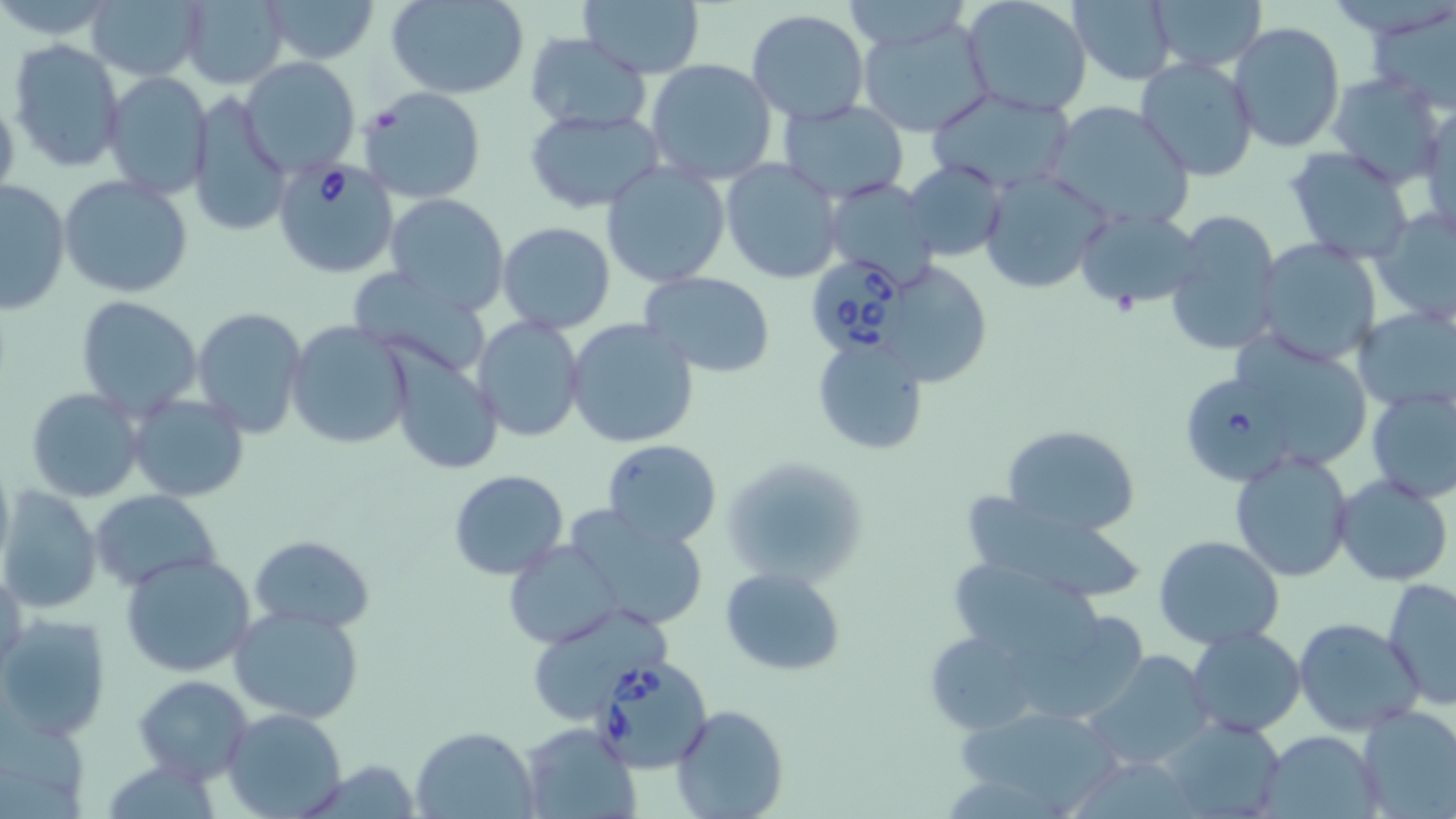 Approximate bounding boxes as [x1, y1, x2, y2] in pixels. Uninfected red blood cell locations: [84, 0, 208, 82], [179, 0, 289, 87], [262, 0, 378, 65], [387, 0, 530, 98], [960, 0, 1093, 117], [1067, 0, 1178, 86], [1151, 0, 1265, 72], [578, 1, 706, 77], [1367, 3, 1454, 114], [746, 10, 871, 125], [857, 13, 996, 138], [1229, 21, 1345, 153], [525, 34, 651, 133], [7, 38, 126, 172], [1134, 55, 1259, 183], [241, 57, 360, 174], [645, 58, 777, 186], [102, 70, 213, 198], [1328, 73, 1448, 190], [361, 87, 486, 204], [187, 90, 291, 236], [924, 90, 1078, 194], [0, 92, 20, 206], [778, 99, 911, 201], [1042, 101, 1196, 233], [1417, 103, 1455, 243], [524, 108, 666, 214], [1284, 145, 1419, 266], [722, 158, 846, 284], [903, 160, 1007, 261], [601, 162, 731, 287], [980, 171, 1111, 294], [59, 175, 194, 300], [0, 178, 71, 314], [823, 178, 941, 290], [385, 194, 508, 311], [1072, 207, 1204, 314], [1370, 207, 1456, 328], [1164, 209, 1284, 358], [497, 222, 617, 333], [1254, 238, 1384, 367], [895, 263, 989, 380], [349, 268, 490, 373], [641, 272, 775, 376], [75, 296, 203, 419], [1351, 305, 1456, 414], [192, 307, 307, 438], [473, 316, 587, 442], [565, 318, 699, 449], [287, 321, 414, 451], [1223, 333, 1383, 476], [810, 334, 928, 456], [386, 345, 504, 478], [25, 386, 145, 504], [1365, 388, 1456, 504], [128, 393, 250, 503], [1003, 424, 1140, 536], [602, 439, 722, 548], [1230, 450, 1355, 584], [0, 452, 15, 578], [722, 461, 857, 622], [447, 469, 570, 581], [1333, 474, 1453, 586], [1, 486, 105, 614], [91, 490, 221, 590], [961, 495, 1143, 602], [559, 507, 706, 629], [250, 534, 374, 632], [1153, 534, 1285, 649], [502, 541, 625, 649], [120, 553, 257, 677], [947, 556, 1103, 663], [1, 562, 26, 681], [721, 567, 848, 675], [1383, 577, 1456, 709], [229, 605, 365, 724], [538, 611, 680, 724], [1, 613, 112, 742], [1294, 617, 1423, 737], [1186, 626, 1307, 736], [924, 629, 1037, 736], [1086, 650, 1214, 769], [133, 674, 253, 783], [672, 704, 788, 818], [959, 704, 1125, 815], [1354, 706, 1456, 815], [223, 707, 347, 818], [1161, 714, 1286, 819], [518, 724, 639, 819], [412, 728, 538, 818], [1256, 730, 1382, 819]. Babesia divergens-infected red blood cell locations: [272, 157, 400, 279], [807, 256, 916, 357], [1175, 369, 1300, 485], [588, 656, 714, 772]. Slide-level diagnosis: Babesia divergens. Image is 1456×819 pixels. Light microscopy. Single field of view. Captured at 1000x magnification. May-Grünwald-Giemsa stain. Thin blood smear.